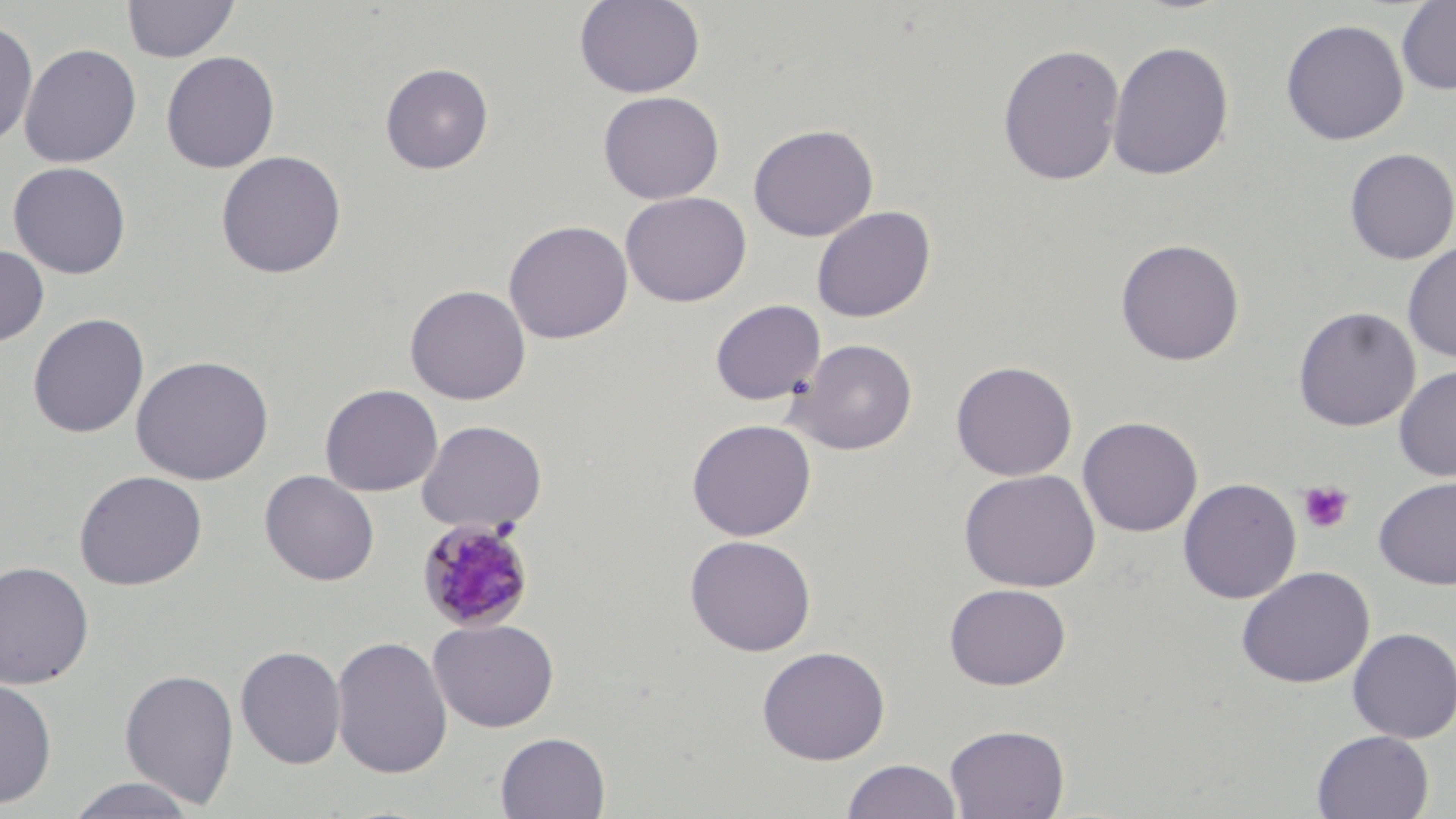

Summary:
  - Coordinate format: approximate bounding boxes as [x1, y1, x2, y2] in pixels
  - Platelet locations: [1298, 481, 1354, 534]
  - Plasmodium malariae-infected red blood cell locations: [416, 516, 538, 634]
  - Uninfected red blood cell locations: [122, 0, 239, 63], [574, 0, 705, 98], [1397, 1, 1456, 96], [0, 18, 38, 148], [1280, 19, 1409, 145], [1106, 41, 1235, 181], [19, 43, 142, 168], [997, 43, 1125, 186], [160, 50, 281, 173], [380, 62, 494, 175], [597, 91, 725, 204], [748, 123, 879, 241], [1343, 148, 1456, 264], [215, 150, 347, 278], [8, 161, 131, 279], [620, 191, 752, 307], [811, 206, 935, 323], [503, 220, 632, 344], [1114, 238, 1245, 366], [1402, 241, 1456, 362], [0, 244, 49, 347], [404, 284, 531, 405], [710, 299, 825, 406], [1293, 306, 1420, 431], [28, 313, 149, 438], [789, 338, 918, 455], [131, 354, 275, 485], [951, 360, 1077, 481], [1394, 364, 1456, 482], [320, 383, 443, 497], [1077, 416, 1203, 537], [416, 419, 547, 534], [686, 419, 817, 541], [958, 468, 1101, 592], [73, 470, 208, 590], [259, 470, 380, 586], [1374, 476, 1456, 589], [1178, 477, 1302, 604], [684, 534, 816, 656], [0, 560, 95, 689], [1236, 566, 1375, 688], [944, 583, 1071, 690], [428, 618, 559, 732], [1347, 627, 1456, 744], [331, 634, 452, 779], [235, 645, 346, 769], [756, 645, 891, 765], [119, 668, 240, 809], [0, 675, 58, 809], [944, 723, 1069, 819], [1311, 730, 1434, 818], [495, 731, 611, 818], [841, 759, 962, 818], [64, 776, 199, 818]
  - Slide-level diagnosis: Plasmodium malariae
  - Magnification: 1000x
  - Modality: optical microscopy
  - Image size: 1456×819 pixels
  - Field of view: single
  - Preparation: thin blood film
  - Stain: May-Grünwald-Giemsa